Classify this cell by malaria status.
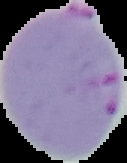

It is parasitized.

Segmented cell region on a black background. From a thin blood smear. Image is 127×163 pixels.